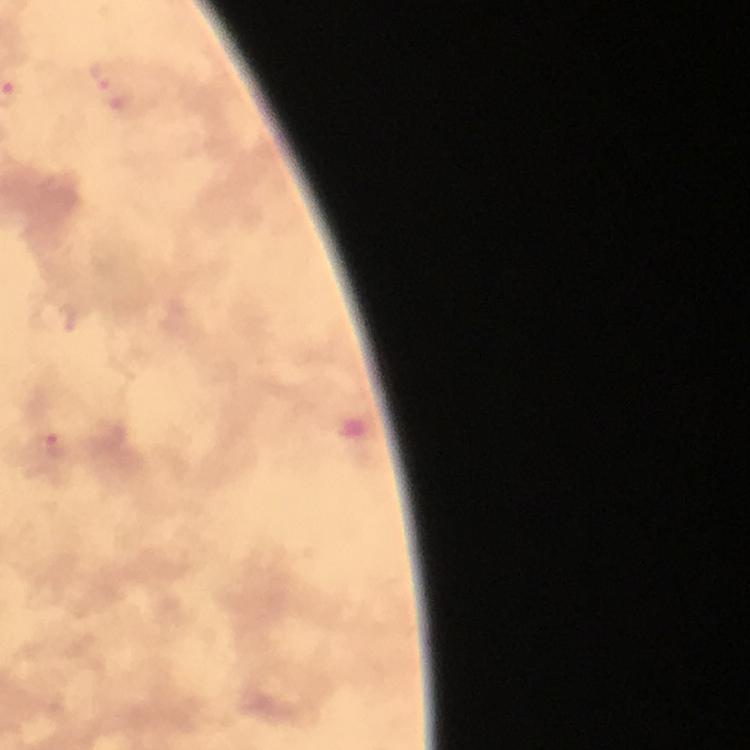

{
  "capture": "smartphone mounted on the microscope",
  "cropped_from": "one field of view",
  "preparation": "thick smear",
  "stain": "Giemsa",
  "context": "from a malaria diagnostic workup",
  "image_size": "750×750 pixels",
  "plasmodium_parasite_locations": "approximate centers as [x, y] in pixels: [102, 74], [53, 445]",
  "immersion_oil": "used",
  "magnification": "100x"
}